Identify the parasite.
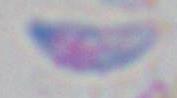

Toxoplasma gondii.

Captured at 1000x magnification. Photomicrograph.